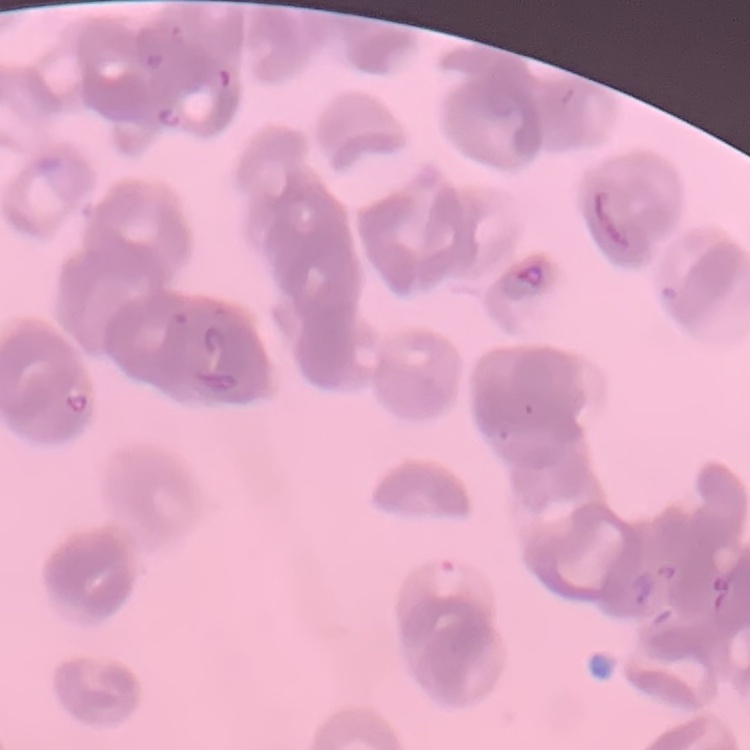

red blood cell morphology = rouleaux formation
preparation = thin blood film
stain = Field's or Giemsa
image type = square crop of a larger photomicrograph